Assess the morphology of the red blood cells.
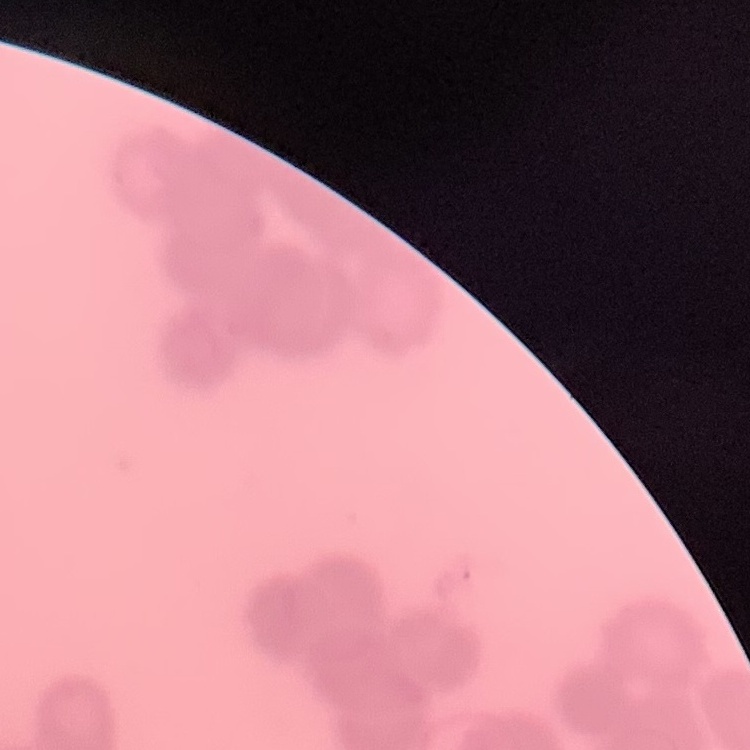
Rouleaux formation.

Summary:
  - Image type: one tile cut from a larger photomicrograph
  - Stain: Field's or Giemsa
  - Preparation: thin peripheral smear